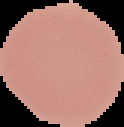

preparation = thin blood smear
result = negative for Plasmodium parasites
image type = cell region segmented out of the field of view; surrounding area masked to black
image size = 124×127 pixels